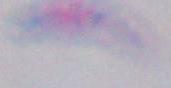

Summary:
  - Magnification: 1000x
  - Identification: Toxoplasma gondii
  - Modality: micrograph